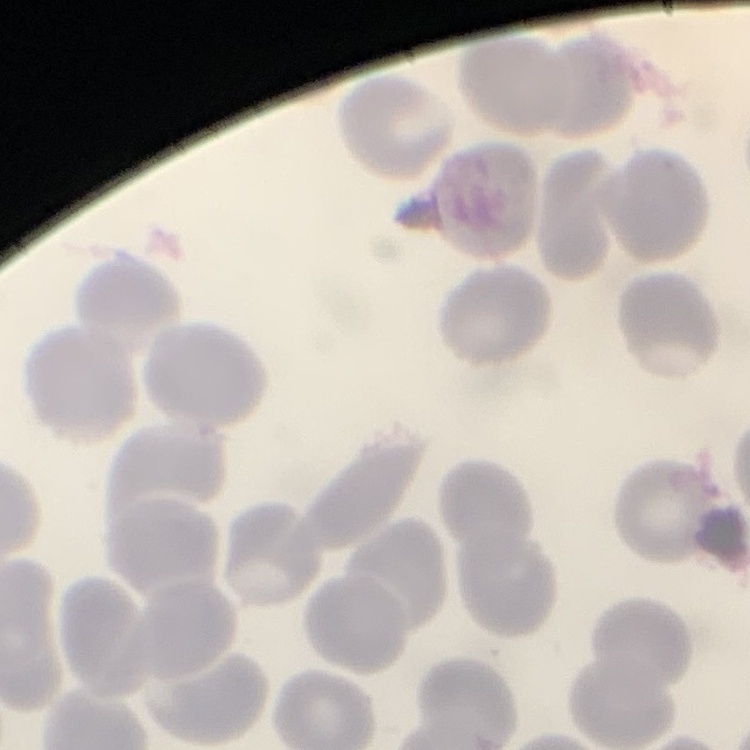
red_blood_cell_morphology: no rouleaux formation
preparation: thin peripheral smear
stain: Field's or Giemsa
image_type: one tile cut from a larger photomicrograph